Identify the parasite.
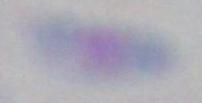
This is Toxoplasma gondii.

Captured at 1000x magnification. Photomicrograph.